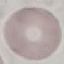

{
  "malaria_status": "uninfected",
  "stain": "Giemsa",
  "preparation": "thin smear",
  "capture": "smartphone camera at the microscope eyepiece",
  "image_type": "automatically extracted cell patch, resized to 64 × 64 pixels"
}